State which parasite is depicted.
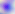
This is Toxoplasma gondii.

modality = micrograph
magnification = 400x